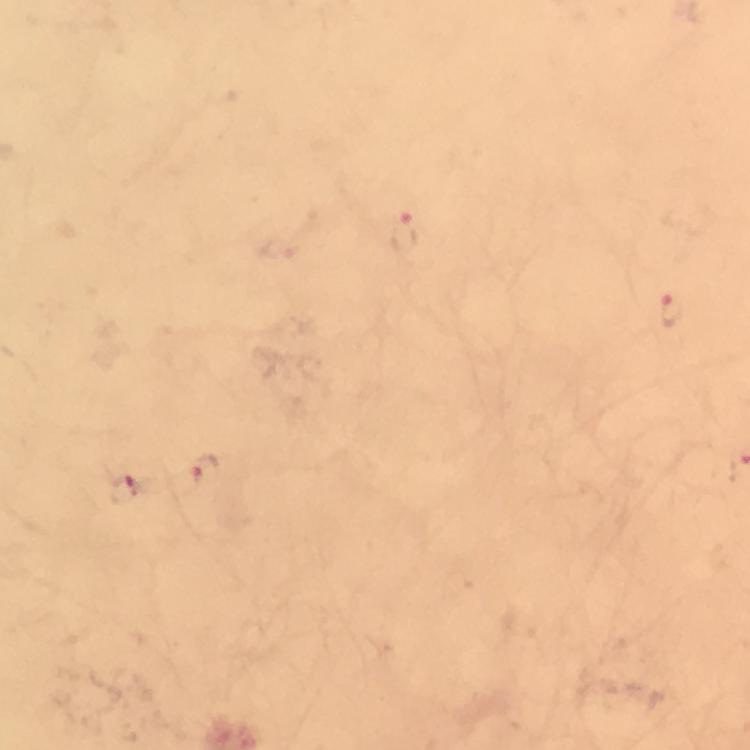
Approximate centers as [x, y] in pixels. Plasmodium parasite locations: [404, 234], [672, 310], [206, 472], [124, 490]. Giemsa stain. Cropped region of a single field of view. Thick blood film. From a diagnostic examination for malaria. Immersion oil was used. Smartphone photograph taken through a microscope. Image is 750×750 pixels. At 100x magnification.